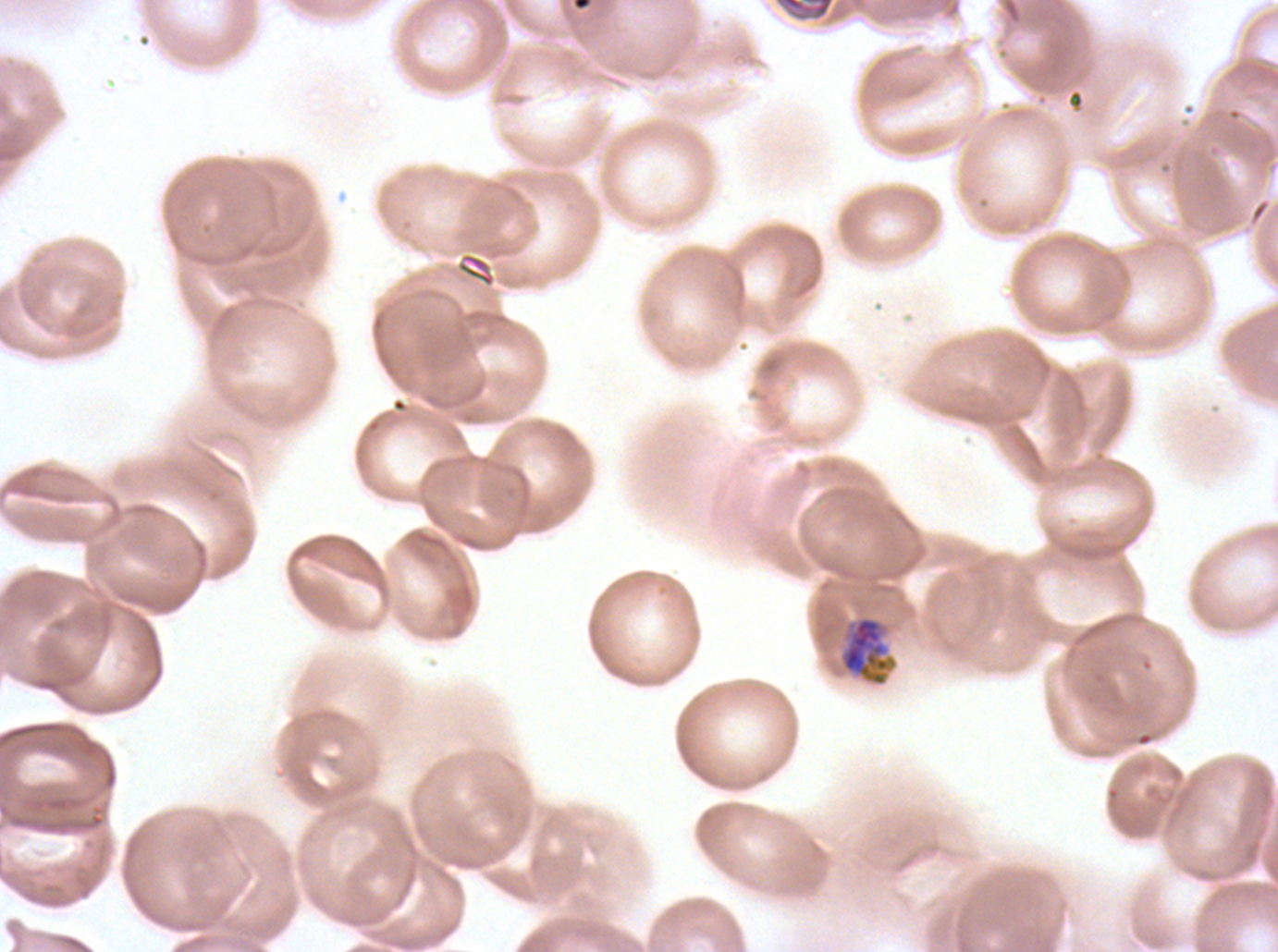
preparation: thin blood film
mid_trophozoite_locations: 'approximate bounding boxes as [x1, y1, x2, y2] in pixels: [838, 615, 897, 687]'
field_of_view: sub-image separated from a larger composite
specimen: ex-vivo P. falciparum culture from a patient in The Gambia, grown for 24 to 48 hours
stain: Giemsa
image_size: 1278×952 pixels